Report the malaria status of this cell.
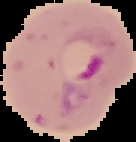
Parasitized.

Image is 136×142 pixels. Cell region segmented out of the field of view; the surrounding area is masked to black. From a thin blood smear.